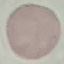

Summary:
  - Result: no malaria parasites seen
  - Stain: Giemsa
  - Capture: smartphone through the microscope eyepiece
  - Preparation: thin blood film
  - Image type: automatically extracted cell patch, resized to 64 × 64 pixels